State the preparation type.
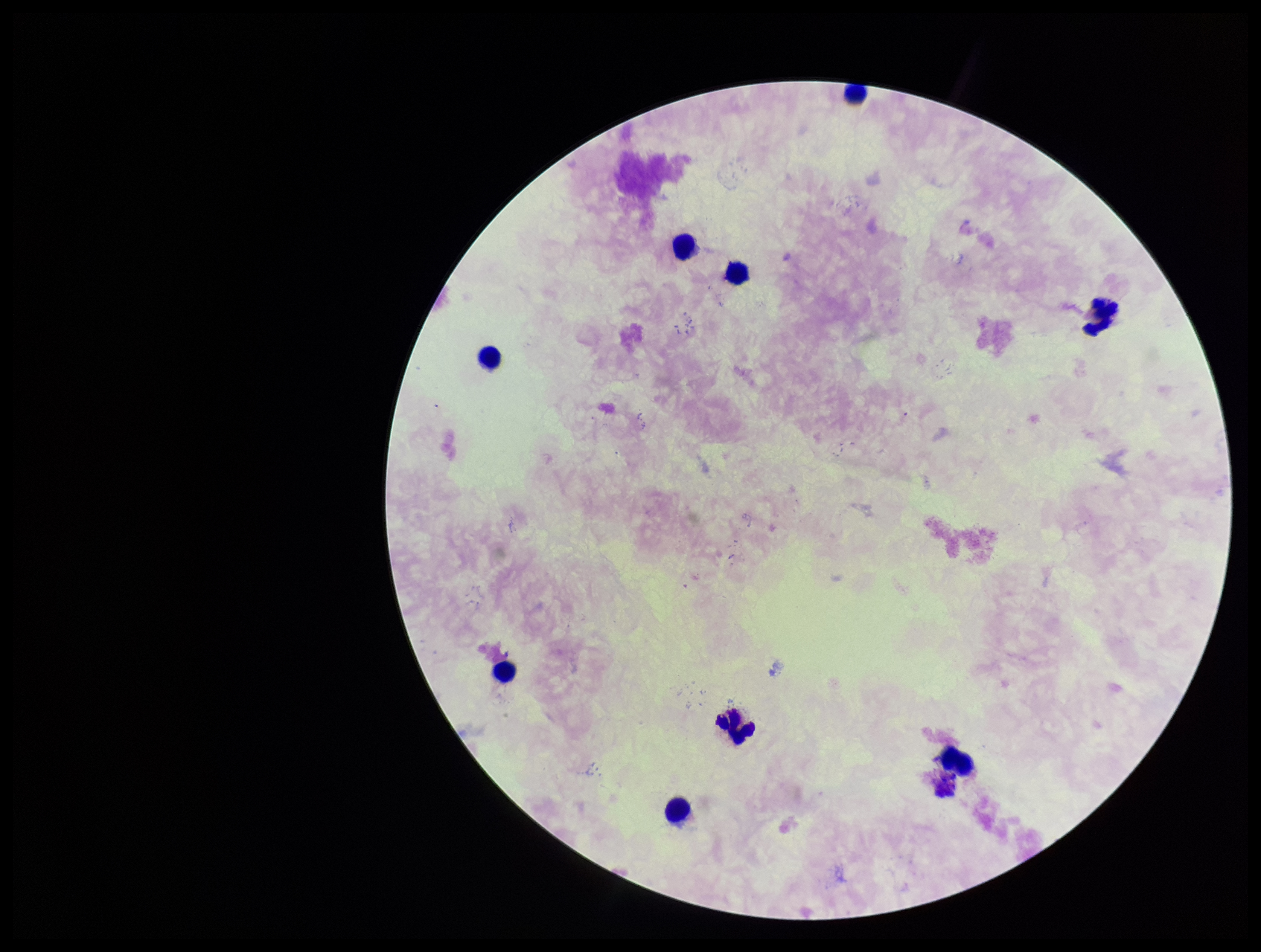
It is a thick blood smear.

patient_malaria_status: negative
field_of_view: one from this slide
parasite_count: 0
image_size: 1261×952 pixels
capture: smartphone photograph through the microscope eyepiece
stain: Giemsa
plasmodium_parasites: none identified
leukocyte_count: 9